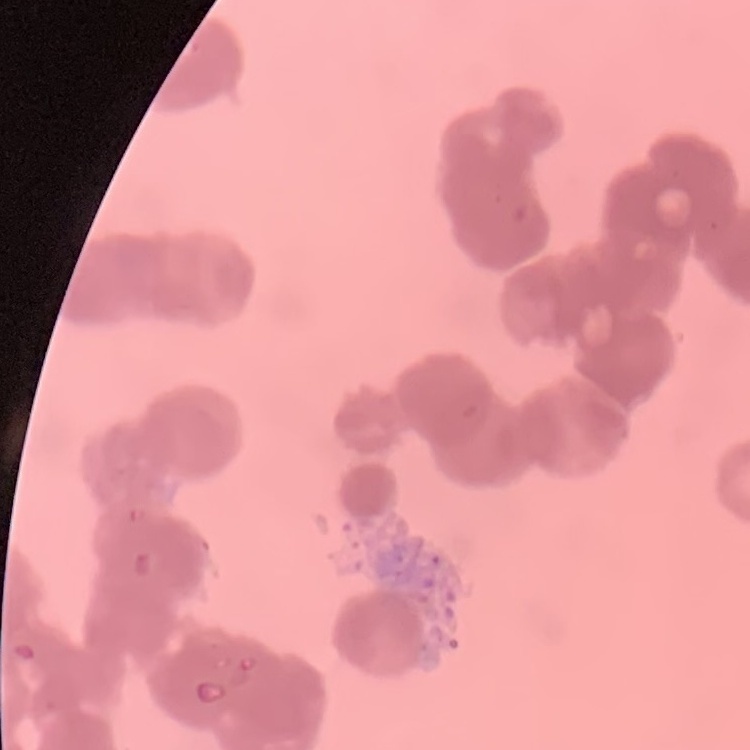

red blood cell morphology = rouleaux formation
preparation = thin blood film
image type = square crop of a larger photomicrograph
stain = Field's or Giemsa